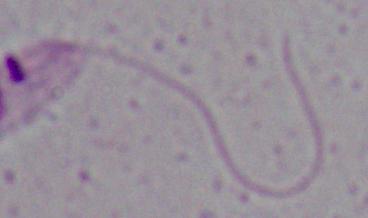

identification = Leishmania
magnification = 1000x
modality = photomicrograph